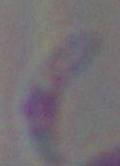
Toxoplasma gondii is seen. Captured at 1000x magnification. Micrograph.